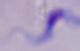

{
  "magnification": "1000x",
  "modality": "micrograph",
  "identification": "trypanosome"
}